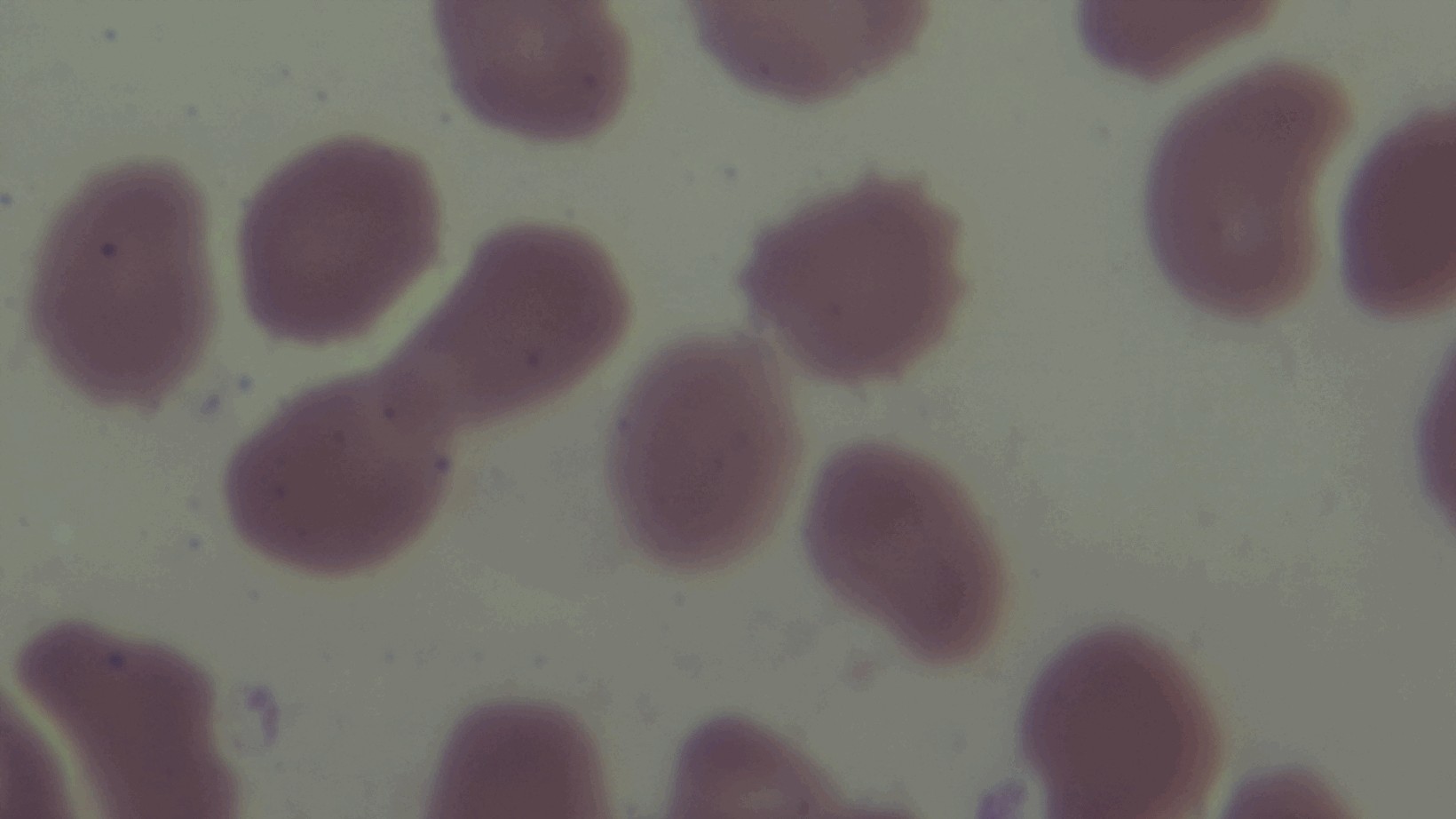
Giemsa-stained. Malaria status: uninfected. 100x oil-immersion objective. Captured with a mounted 4K digital camera. Preparation: thin blood film. Photomicrograph. Single field of view.